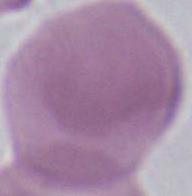

Photomicrograph. 1000x magnification. An erythrocyte is seen.